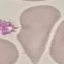

result = no malaria parasites detected
image type = cell patch, automatically extracted from a larger field of view and resized to 64 × 64 pixels
capture = smartphone through the microscope eyepiece
preparation = thin blood film
stain = Giemsa